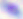

Summary:
  - Magnification: 400x
  - Modality: photomicrograph
  - Identification: Toxoplasma gondii